State the blood parasite species.
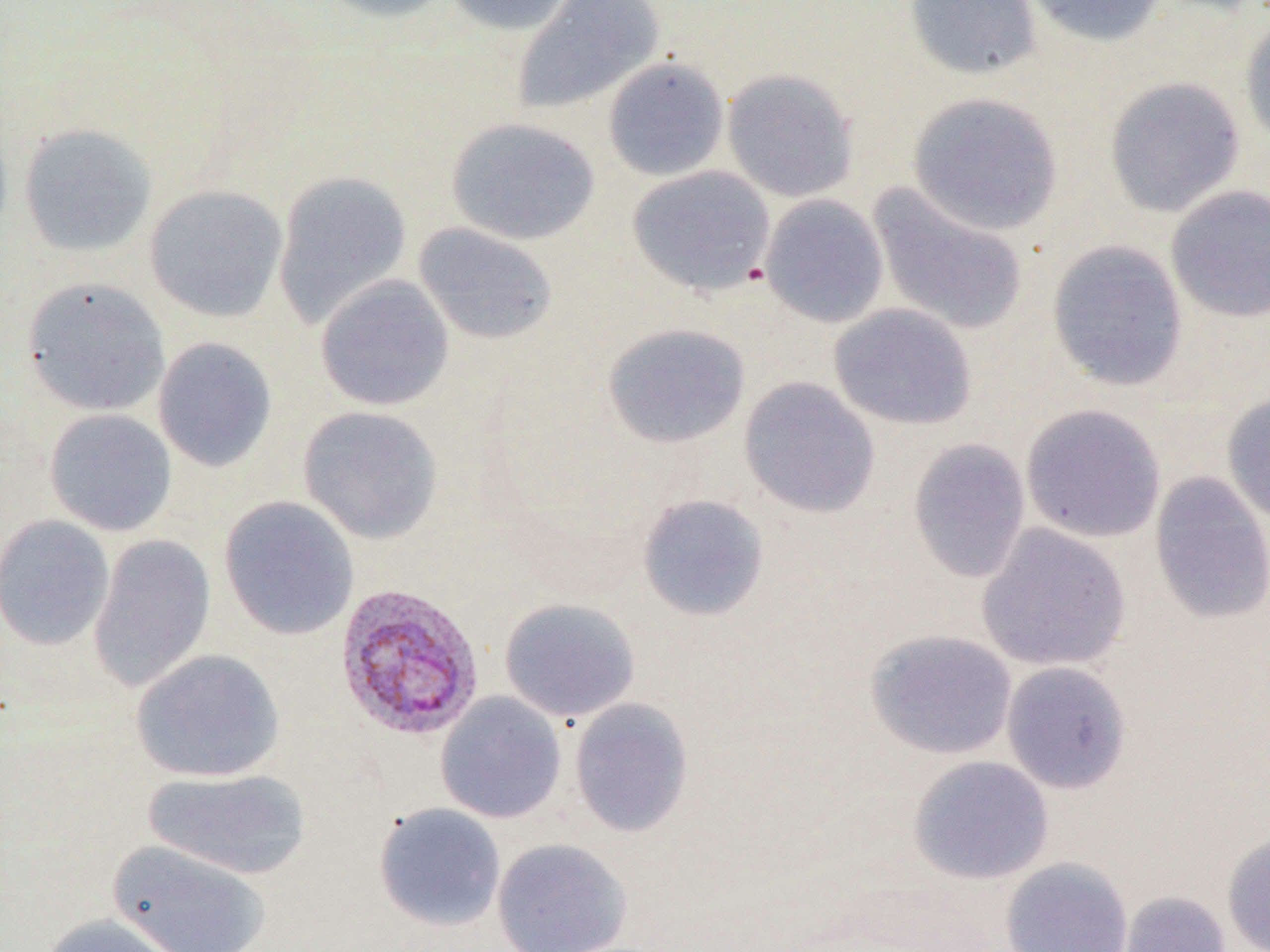

Plasmodium vivax.

Approximate bounding boxes as (x1, y1, x2, y2) in pixels. Plasmodium vivax-infected red blood cell locations: (334, 582, 486, 741). Uninfected red blood cell locations: (315, 0, 456, 23), (443, 0, 578, 36), (511, 0, 666, 116), (904, 0, 1043, 80), (1021, 0, 1169, 48), (1239, 14, 1270, 149), (602, 56, 729, 182), (721, 68, 859, 203), (1104, 76, 1246, 218), (907, 91, 1064, 235), (445, 117, 601, 245), (17, 122, 157, 257), (627, 165, 776, 296), (271, 170, 413, 329), (867, 182, 1030, 338), (1166, 184, 1270, 323), (143, 185, 288, 322), (759, 193, 889, 328), (413, 222, 558, 345), (1046, 238, 1189, 391), (315, 274, 455, 411), (21, 276, 171, 417), (828, 303, 977, 430), (602, 322, 750, 448), (153, 337, 277, 472), (739, 377, 881, 518), (1221, 394, 1270, 524), (1020, 403, 1166, 543), (297, 405, 444, 544), (43, 408, 178, 537), (907, 438, 1031, 584), (1149, 472, 1270, 624), (637, 493, 770, 621), (218, 495, 359, 640), (0, 514, 115, 651), (976, 523, 1132, 672), (87, 534, 216, 692), (499, 598, 640, 722), (865, 628, 1018, 760), (130, 648, 286, 783), (1001, 661, 1132, 793), (435, 691, 567, 824), (569, 697, 694, 837), (908, 755, 1054, 885), (142, 768, 312, 880), (373, 802, 506, 931), (1221, 830, 1270, 952), (491, 837, 633, 952), (107, 839, 270, 952), (1000, 857, 1133, 952), (1118, 890, 1232, 952), (39, 913, 184, 952). Thin blood film. Single field of view. Image is 1270×952 pixels. Captured at 1000x magnification. Optical microscopy.